Classify this cell by malaria status.
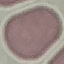

It is uninfected.

Summary:
  - Stain: Giemsa
  - Preparation: thin blood film
  - Image type: automatically extracted cell patch, resized to 64 × 64 pixels
  - Capture: smartphone camera at the microscope eyepiece